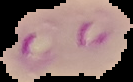
From a thin blood smear. Cell region segmented out of the field of view; the surrounding area is masked to black. Image is 133×82 pixels. Result: malaria parasites identified.